Identify the parasite.
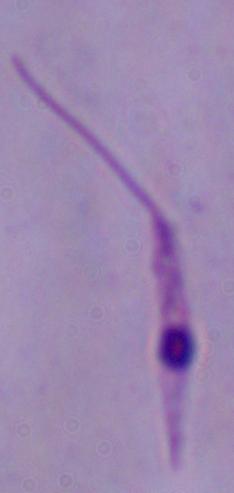
Leishmania.

Micrograph. 1000x magnification.